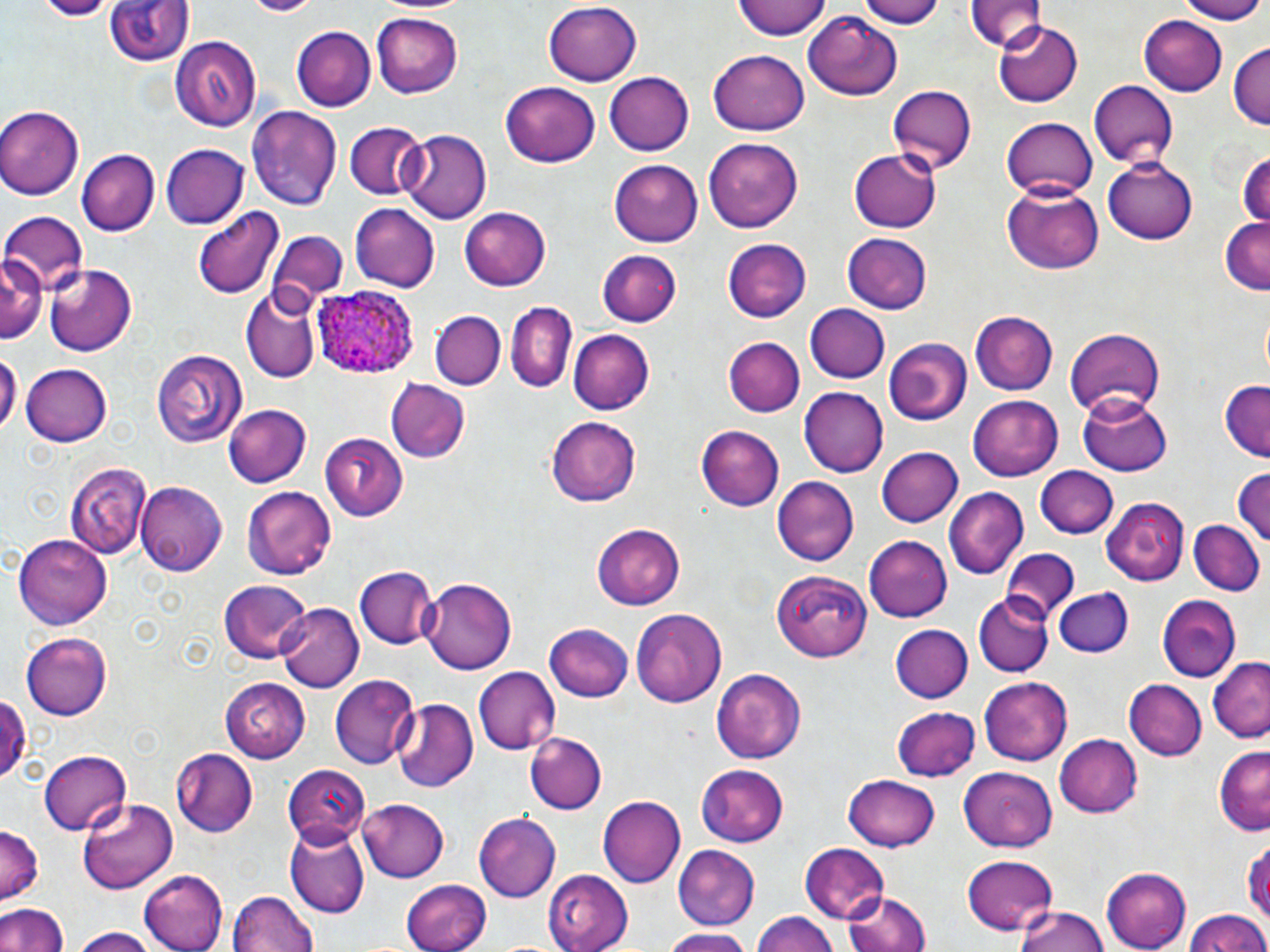
{
  "slide_level_diagnosis": "Plasmodium ovale",
  "uninfected_red_blood_cell_locations": "approximate bounding boxes as (x1,y1)-(x2,y2) corner pairs in pixels: (35,0)-(110,20), (105,0)-(193,69), (735,0)-(830,41), (853,0)-(944,27), (966,0)-(1045,52), (1172,0)-(1269,22), (543,2)-(641,87), (804,9)-(903,99), (373,13)-(464,97), (1141,15)-(1227,95), (994,19)-(1084,107), (293,28)-(375,110), (169,36)-(261,134), (1228,43)-(1269,131), (707,50)-(811,136), (605,73)-(694,156), (1088,80)-(1180,170), (501,82)-(600,168), (888,84)-(977,172), (0,104)-(85,199), (248,106)-(341,211), (1002,115)-(1098,201), (343,121)-(427,201), (399,130)-(494,224), (702,137)-(803,233), (161,144)-(248,230), (848,147)-(945,232), (1235,147)-(1270,231), (76,149)-(159,235), (1102,157)-(1197,244), (609,160)-(703,246), (1001,185)-(1105,275), (350,203)-(438,291), (457,206)-(551,291), (193,207)-(283,299), (1,211)-(89,297), (1219,217)-(1270,294), (270,228)-(348,304), (840,233)-(934,314), (723,239)-(811,323), (597,248)-(682,324), (1,251)-(43,345), (42,264)-(137,357), (241,288)-(322,383), (504,301)-(576,392), (806,303)-(890,384), (430,312)-(507,389), (968,312)-(1058,396), (1063,327)-(1166,421), (567,328)-(654,415), (724,336)-(804,417), (883,336)-(973,426), (0,348)-(18,440), (151,348)-(246,448), (20,362)-(112,448), (387,379)-(469,462), (1219,382)-(1269,461), (799,387)-(889,477), (1079,390)-(1173,474), (966,394)-(1062,481), (225,404)-(313,487), (548,415)-(642,504), (697,424)-(783,511), (318,430)-(408,522), (320,432)-(408,521), (874,446)-(962,528), (64,460)-(150,557), (1035,465)-(1117,539), (1232,466)-(1269,550), (772,476)-(860,567), (137,481)-(228,575), (241,485)-(335,581), (946,488)-(1029,580), (1101,497)-(1192,585), (1189,520)-(1264,596), (591,523)-(686,610), (15,533)-(115,626), (865,537)-(953,622), (1001,551)-(1080,621), (354,567)-(437,649), (773,569)-(871,661), (418,577)-(516,676), (217,578)-(310,666), (1054,587)-(1134,659), (974,593)-(1053,676), (1157,593)-(1240,681), (278,603)-(363,691), (630,607)-(727,708), (890,622)-(973,704), (545,623)-(634,704), (20,632)-(114,719), (1208,658)-(1268,743), (473,667)-(559,754), (710,667)-(807,764), (332,674)-(419,767), (979,675)-(1073,766), (1124,677)-(1207,761), (221,678)-(307,761), (0,692)-(28,786), (393,698)-(478,793), (886,700)-(1065,776), (893,707)-(982,781), (524,730)-(609,815), (1056,735)-(1143,818), (1213,746)-(1268,834), (170,747)-(258,834), (40,749)-(133,835), (281,765)-(369,844), (694,765)-(787,847), (957,767)-(1057,852), (841,774)-(941,852), (598,795)-(684,886), (77,798)-(179,896), (357,798)-(450,882), (474,811)-(560,901), (282,823)-(369,919), (0,825)-(43,904), (1247,840)-(1270,925), (800,845)-(889,922), (673,846)-(761,929), (962,855)-(1058,935), (141,866)-(228,950), (1100,868)-(1191,950), (543,869)-(633,951), (402,878)-(490,952), (843,885)-(933,952), (229,889)-(319,952), (0,900)-(67,952), (1015,905)-(1110,952), (749,909)-(842,952), (1184,909)-(1269,952), (69,927)-(159,952), (659,929)-(758,952)",
  "magnification": "1000x",
  "preparation": "thin blood smear",
  "modality": "light microscopy",
  "plasmodium_ovale_infected_red_blood_cell_locations": "approximate bounding boxes as (x1,y1)-(x2,y2) corner pairs in pixels: (311,284)-(421,375)",
  "stain": "May-Grünwald-Giemsa",
  "image_size": "1270×952 pixels",
  "field_of_view": "single"
}